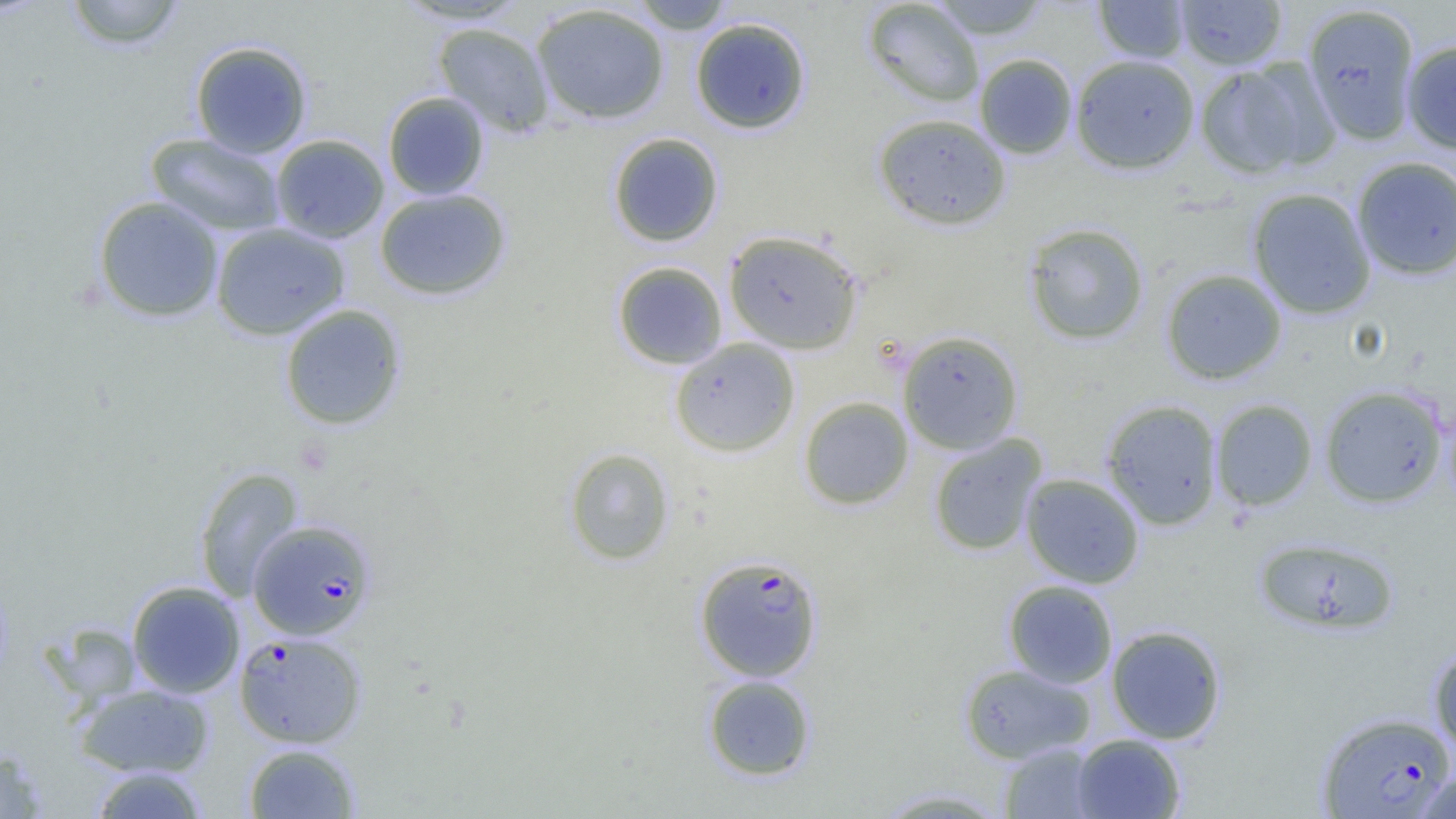

slide-level diagnosis = Plasmodium falciparum
field of view = single
uninfected red blood cell locations = approximate bounding boxes as [x1, y1, x2, y2] in pixels: [64, 0, 187, 51], [391, 0, 531, 25], [630, 0, 735, 33], [862, 0, 985, 107], [928, 0, 1051, 40], [1094, 0, 1191, 63], [1174, 0, 1287, 70], [1302, 3, 1421, 145], [531, 4, 669, 124], [690, 17, 812, 134], [432, 22, 554, 136], [1401, 39, 1456, 153], [190, 40, 312, 158], [974, 53, 1078, 159], [1070, 54, 1200, 174], [1194, 61, 1323, 179], [383, 92, 490, 200], [873, 113, 1011, 231], [145, 133, 286, 237], [608, 133, 724, 247], [270, 134, 389, 244], [1351, 156, 1456, 280], [374, 188, 511, 300], [1247, 188, 1376, 319], [93, 196, 224, 322], [1023, 222, 1150, 345], [210, 223, 350, 340], [723, 229, 864, 354], [612, 261, 728, 369], [1161, 268, 1287, 385], [279, 304, 407, 430], [897, 330, 1024, 454], [669, 338, 801, 457], [1319, 386, 1448, 507], [798, 396, 914, 510], [1101, 399, 1223, 530], [1210, 399, 1318, 511], [928, 434, 1047, 557], [564, 447, 675, 566], [193, 466, 304, 601], [1021, 473, 1144, 589], [1253, 536, 1399, 635], [1003, 580, 1118, 689], [126, 581, 245, 698], [45, 622, 142, 705], [1106, 625, 1226, 744], [1429, 646, 1456, 759], [959, 663, 1095, 763], [703, 675, 816, 780], [74, 683, 214, 778], [1071, 733, 1186, 818], [243, 743, 361, 818], [1000, 743, 1102, 819], [0, 747, 48, 819], [89, 766, 209, 818], [1412, 768, 1456, 818], [871, 788, 1013, 818]
Plasmodium falciparum-infected red blood cell locations = approximate bounding boxes as [x1, y1, x2, y2] in pixels: [247, 518, 377, 640], [694, 554, 824, 681], [234, 630, 366, 748], [1317, 711, 1455, 817]
magnification = 1000x
image size = 1456×819 pixels
preparation = thin blood film
modality = light microscopy